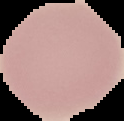

malaria status = uninfected
image size = 124×121 pixels
preparation = thin blood smear
image type = segmented cell region on a black background